State which cell type is depicted.
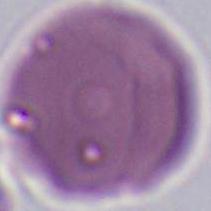

An erythrocyte.

{
  "magnification": "1000x",
  "modality": "photomicrograph"
}